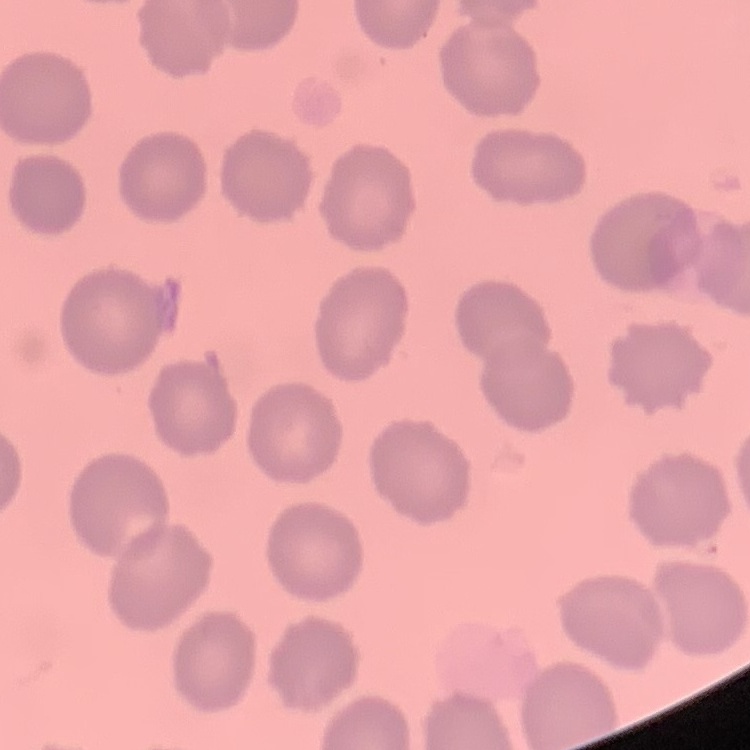

Summary:
  - Erythrocyte morphology: no rouleaux formation
  - Stain: Field's or Giemsa
  - Image type: one tile cut from a larger photomicrograph
  - Preparation: thin peripheral smear